Outline each blood parasite and name the species.
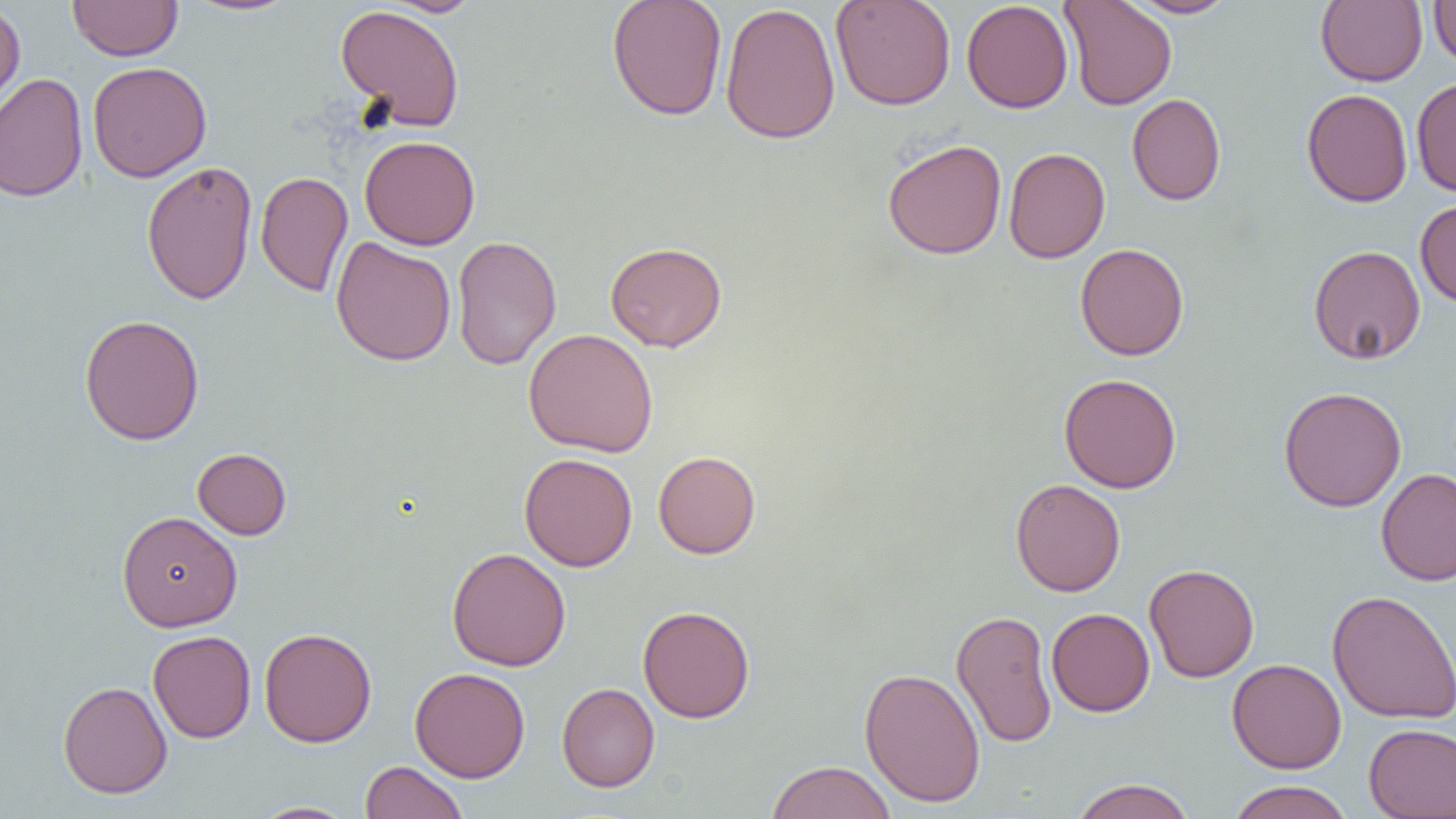

No blood parasites observed.

Approximate bounding boxes as (x1, y1, x2, y2) in pixels. Uninfected red blood cell locations: (67, 0, 183, 61), (182, 0, 301, 17), (380, 0, 485, 17), (607, 0, 728, 120), (830, 0, 956, 111), (961, 0, 1073, 113), (1059, 0, 1177, 110), (1122, 0, 1237, 18), (1315, 0, 1428, 87), (1428, 0, 1456, 68), (0, 2, 26, 119), (720, 2, 840, 145), (334, 5, 466, 132), (87, 61, 211, 182), (0, 73, 88, 202), (1410, 77, 1456, 196), (1301, 88, 1413, 207), (1127, 93, 1227, 206), (360, 135, 481, 250), (882, 138, 1007, 260), (1003, 147, 1110, 263), (141, 159, 258, 305), (255, 171, 353, 296), (1415, 200, 1456, 308), (451, 235, 562, 371), (330, 236, 456, 366), (605, 241, 727, 352), (1075, 243, 1189, 360), (1308, 245, 1426, 364), (79, 314, 205, 445), (523, 328, 658, 457), (1059, 373, 1182, 493), (1278, 386, 1407, 511), (192, 447, 292, 540), (653, 451, 761, 559), (519, 453, 637, 571), (1377, 468, 1456, 586), (1010, 478, 1125, 596), (117, 510, 242, 632), (447, 547, 571, 671), (1144, 563, 1259, 682), (1327, 590, 1456, 725), (637, 605, 755, 723), (951, 608, 1057, 748), (1047, 608, 1155, 716), (259, 627, 377, 747), (147, 630, 256, 743), (1228, 658, 1347, 773), (410, 667, 530, 783), (859, 667, 986, 808), (58, 681, 172, 798), (557, 683, 660, 792), (1363, 724, 1456, 818), (360, 760, 468, 819), (764, 761, 897, 819), (1069, 778, 1196, 819), (1225, 780, 1355, 819), (250, 801, 358, 818). Slide-level diagnosis: negative for blood parasites. Thin blood smear. Optical microscopy. Image is 1456×819 pixels. Single field of view. Captured at 1000x magnification.